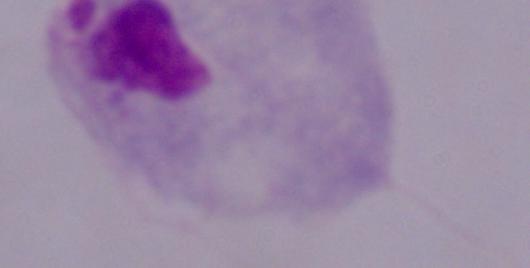
{
  "identification": "trichomonad",
  "modality": "photomicrograph",
  "magnification": "1000x"
}